Name the parasite shown.
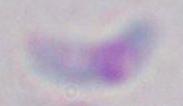

Toxoplasma gondii.

Photomicrograph. Captured at 1000x magnification.